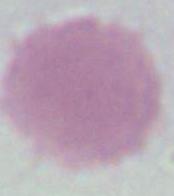
Summary:
  - Modality: micrograph
  - Magnification: 1000x
  - Identification: red blood cell